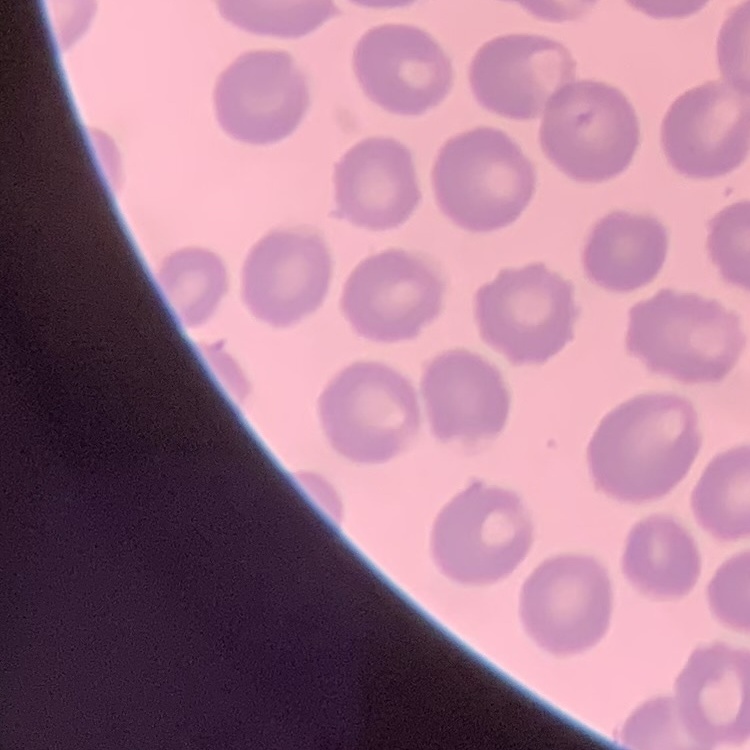
The red blood cells show no rouleaux formation. Thin peripheral smear. Field's or Giemsa stain. One tile cut from a larger photomicrograph.